State the blood parasite species.
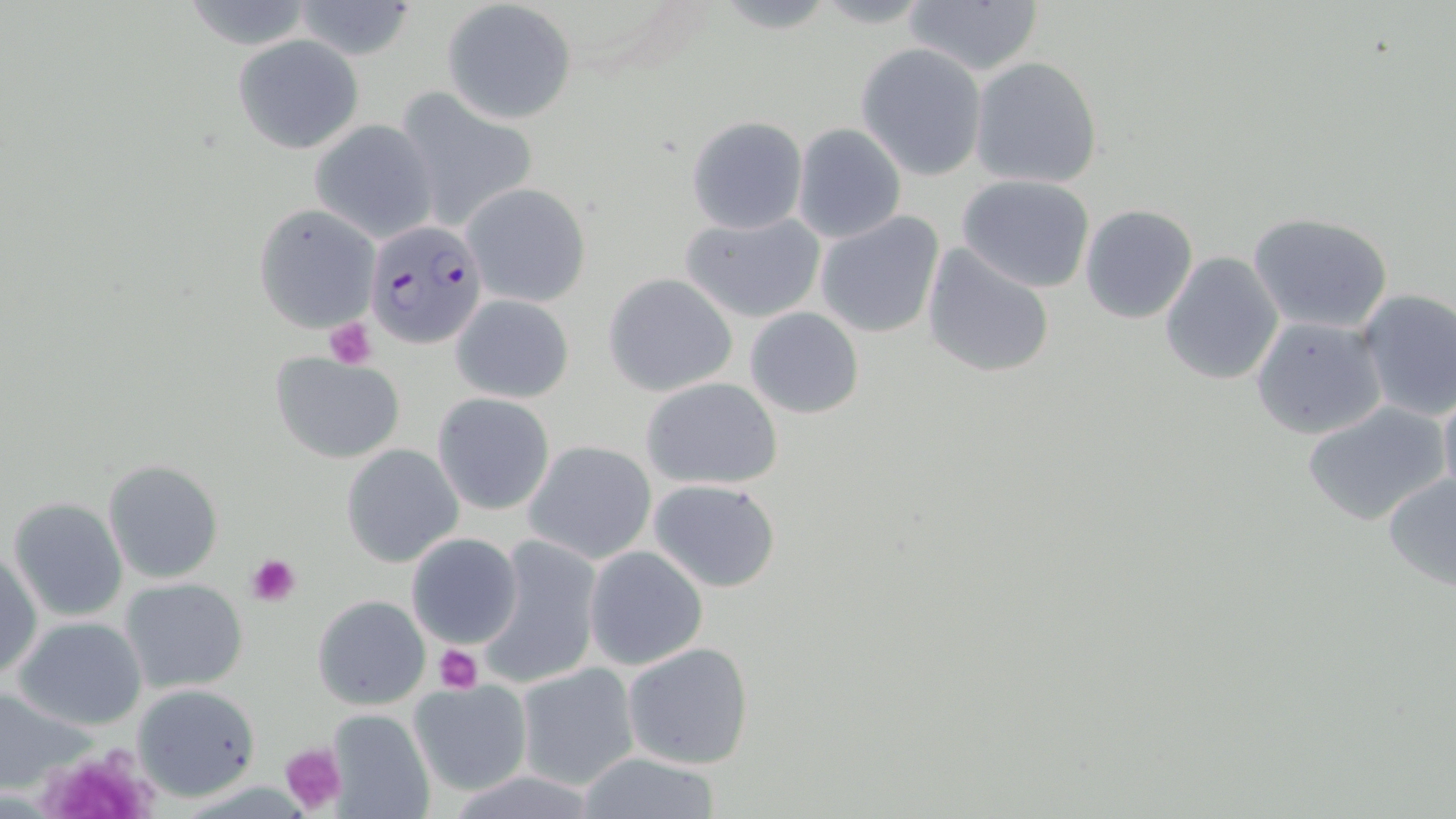

Plasmodium falciparum.

Summary:
  - Coordinate format: approximate bounding boxes as [x1, y1, x2, y2] in pixels
  - Plasmodium falciparum-infected red blood cell locations: [363, 217, 485, 349]
  - Platelet locations: [324, 318, 379, 368], [245, 553, 302, 607], [432, 644, 485, 694], [279, 742, 347, 815], [47, 756, 159, 819]
  - Uninfected red blood cell locations: [289, 0, 420, 60], [181, 1, 318, 50], [442, 1, 577, 125], [904, 1, 1044, 77], [232, 35, 364, 155], [856, 43, 988, 179], [970, 56, 1103, 190], [392, 87, 540, 231], [686, 116, 807, 234], [308, 118, 439, 243], [794, 123, 906, 243], [957, 173, 1095, 293], [462, 182, 590, 309], [253, 203, 380, 333], [1079, 204, 1199, 325], [816, 211, 945, 339], [680, 212, 826, 323], [1248, 212, 1394, 333], [920, 243, 1056, 380], [1159, 251, 1284, 386], [603, 273, 738, 396], [1354, 288, 1456, 421], [449, 293, 575, 404], [745, 306, 864, 420], [1249, 316, 1387, 440], [270, 351, 406, 462], [641, 377, 784, 490], [1437, 379, 1456, 506], [432, 392, 556, 516], [1304, 401, 1448, 526], [523, 439, 657, 563], [339, 443, 463, 568], [103, 458, 224, 585], [1381, 471, 1456, 592], [648, 478, 781, 593], [8, 497, 128, 623], [406, 532, 524, 649], [475, 533, 602, 690], [1, 544, 41, 683], [584, 546, 707, 670], [119, 577, 249, 695], [313, 595, 430, 710], [12, 616, 148, 731], [622, 641, 755, 771], [514, 661, 640, 791], [407, 679, 534, 797], [135, 683, 260, 801], [0, 685, 94, 793], [324, 709, 436, 819], [569, 753, 729, 818]
  - Modality: light microscopy
  - Field of view: one of a larger specimen
  - Stain: May-Grünwald-Giemsa
  - Preparation: thin blood smear
  - Magnification: 1000x
  - Image size: 1456×819 pixels